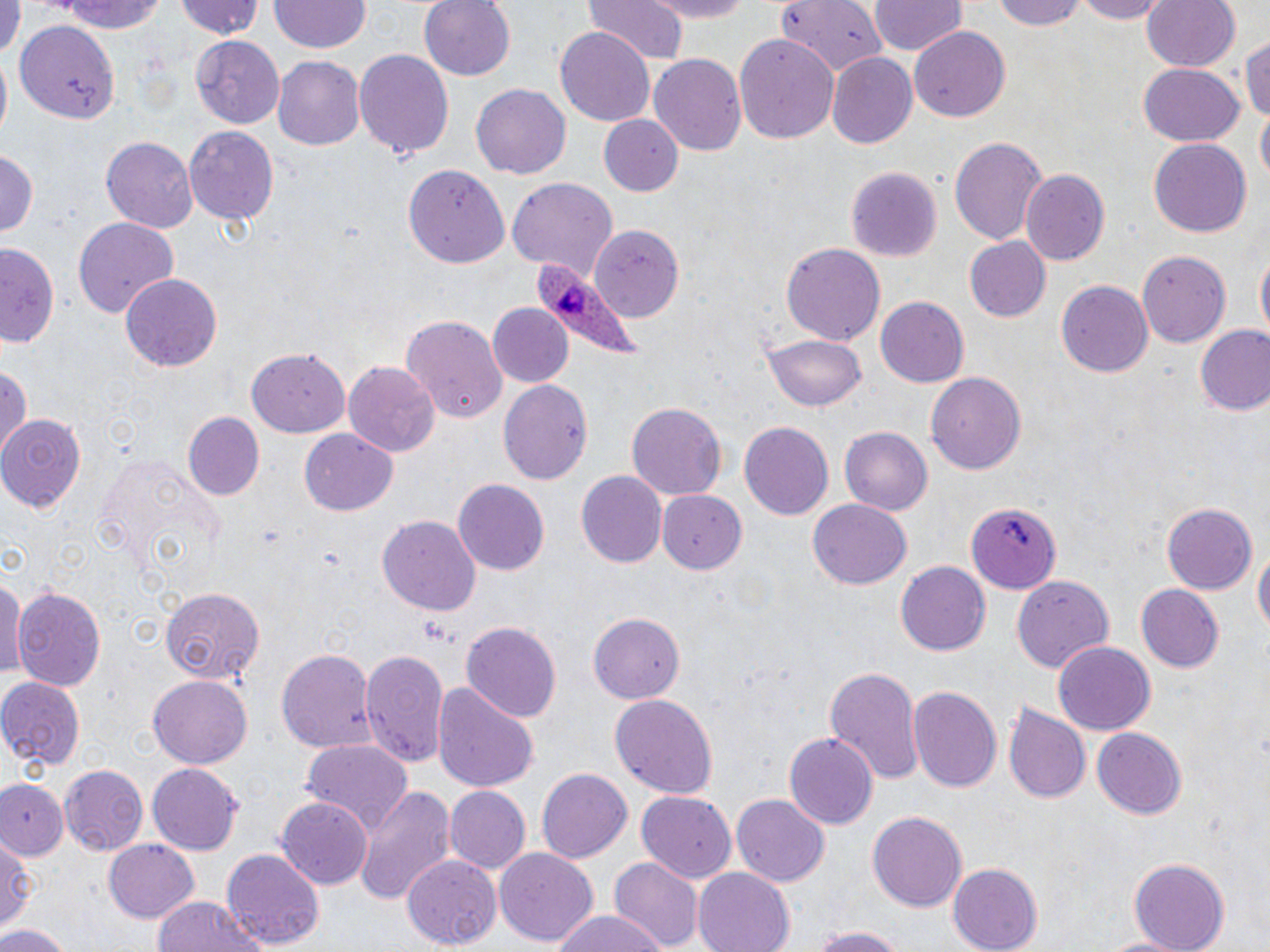

Approximate bounding boxes as [x1, y1, x2, y2] in pixels. Uninfected red blood cell locations: [52, 0, 172, 34], [172, 0, 266, 41], [419, 0, 516, 81], [585, 0, 689, 64], [635, 0, 758, 22], [775, 0, 888, 74], [992, 0, 1090, 30], [1068, 0, 1173, 23], [1141, 0, 1240, 73], [0, 1, 21, 63], [869, 1, 965, 58], [268, 2, 369, 54], [15, 22, 119, 121], [909, 26, 1010, 123], [556, 28, 653, 126], [1241, 29, 1270, 126], [734, 34, 840, 146], [191, 35, 286, 126], [355, 48, 454, 161], [649, 53, 749, 155], [828, 53, 918, 150], [274, 55, 369, 150], [1136, 64, 1244, 147], [472, 84, 569, 180], [599, 113, 683, 196], [184, 123, 278, 223], [949, 135, 1048, 245], [101, 136, 198, 231], [1150, 139, 1251, 238], [0, 148, 39, 239], [403, 161, 507, 269], [845, 165, 943, 262], [1022, 171, 1109, 265], [507, 179, 616, 276], [71, 216, 180, 320], [592, 229, 681, 316], [962, 235, 1051, 323], [0, 240, 60, 348], [782, 243, 884, 349], [1254, 249, 1268, 347], [1137, 250, 1230, 348], [119, 270, 222, 372], [1056, 281, 1153, 379], [875, 296, 968, 388], [485, 303, 575, 388], [401, 314, 506, 423], [1195, 327, 1270, 417], [766, 331, 867, 409], [247, 348, 349, 436], [345, 361, 438, 458], [0, 362, 30, 454], [928, 372, 1026, 477], [497, 378, 592, 485], [627, 400, 726, 497], [184, 412, 264, 498], [2, 414, 83, 513], [739, 422, 834, 522], [838, 426, 933, 514], [297, 428, 398, 518], [577, 471, 667, 569], [452, 480, 549, 576], [659, 490, 748, 573], [808, 498, 913, 591], [1162, 502, 1258, 596], [967, 503, 1062, 594], [377, 515, 482, 614], [1251, 540, 1269, 643], [897, 562, 991, 656], [0, 568, 24, 685], [1011, 576, 1114, 672], [1137, 585, 1224, 673], [11, 587, 108, 691], [159, 588, 265, 684], [590, 611, 689, 703], [461, 619, 563, 722], [1052, 641, 1155, 736], [275, 648, 377, 753], [359, 648, 450, 773], [823, 666, 923, 786], [1, 674, 84, 770], [149, 674, 251, 768], [433, 680, 539, 795], [909, 683, 1003, 795], [608, 694, 720, 799], [1006, 702, 1093, 803], [1092, 729, 1187, 819], [782, 731, 878, 829], [301, 740, 412, 839], [58, 763, 146, 855], [148, 765, 243, 854], [535, 767, 632, 864], [0, 779, 70, 860], [352, 785, 455, 906], [445, 787, 529, 874], [637, 791, 735, 885], [732, 795, 829, 887], [277, 796, 373, 889], [867, 811, 968, 911], [0, 832, 36, 937], [104, 838, 198, 923], [222, 848, 323, 950], [496, 849, 597, 948], [402, 854, 500, 951], [609, 858, 702, 950], [1127, 858, 1232, 951], [946, 863, 1043, 952], [694, 867, 795, 952], [151, 896, 265, 952], [547, 910, 674, 952], [0, 921, 75, 952], [804, 922, 912, 952], [1095, 931, 1193, 951]. Platelet locations: [420, 617, 452, 647]. Plasmodium ovale-infected red blood cell locations: [529, 262, 638, 356]. Slide-level diagnosis: Plasmodium ovale. Thin blood smear. Image is 1270×952 pixels. Single field of view. May-Grünwald-Giemsa-stained preparation. Light microscopy. 1000x magnification.